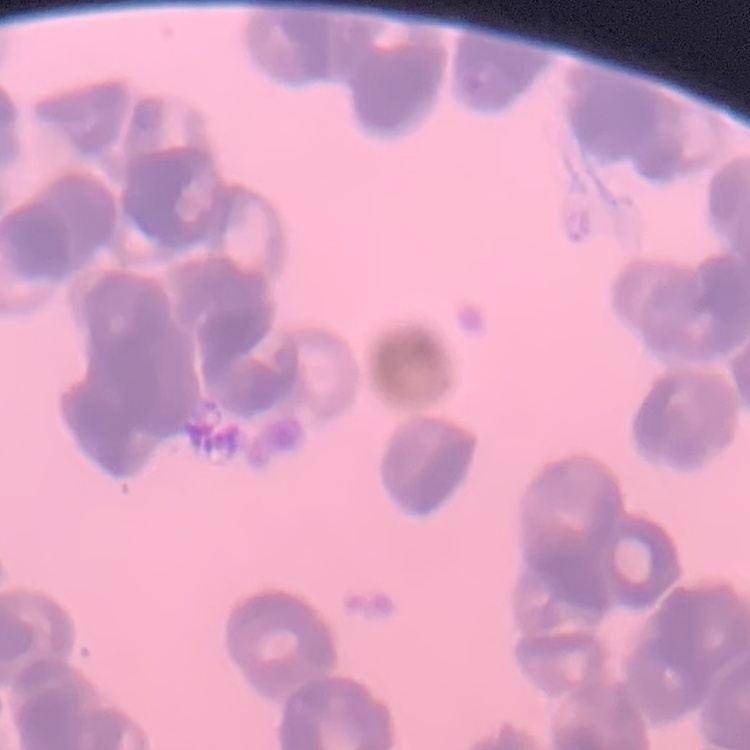
red blood cell morphology = rouleaux formation
preparation = thin peripheral smear
stain = Field's or Giemsa
image type = square crop of a larger photomicrograph